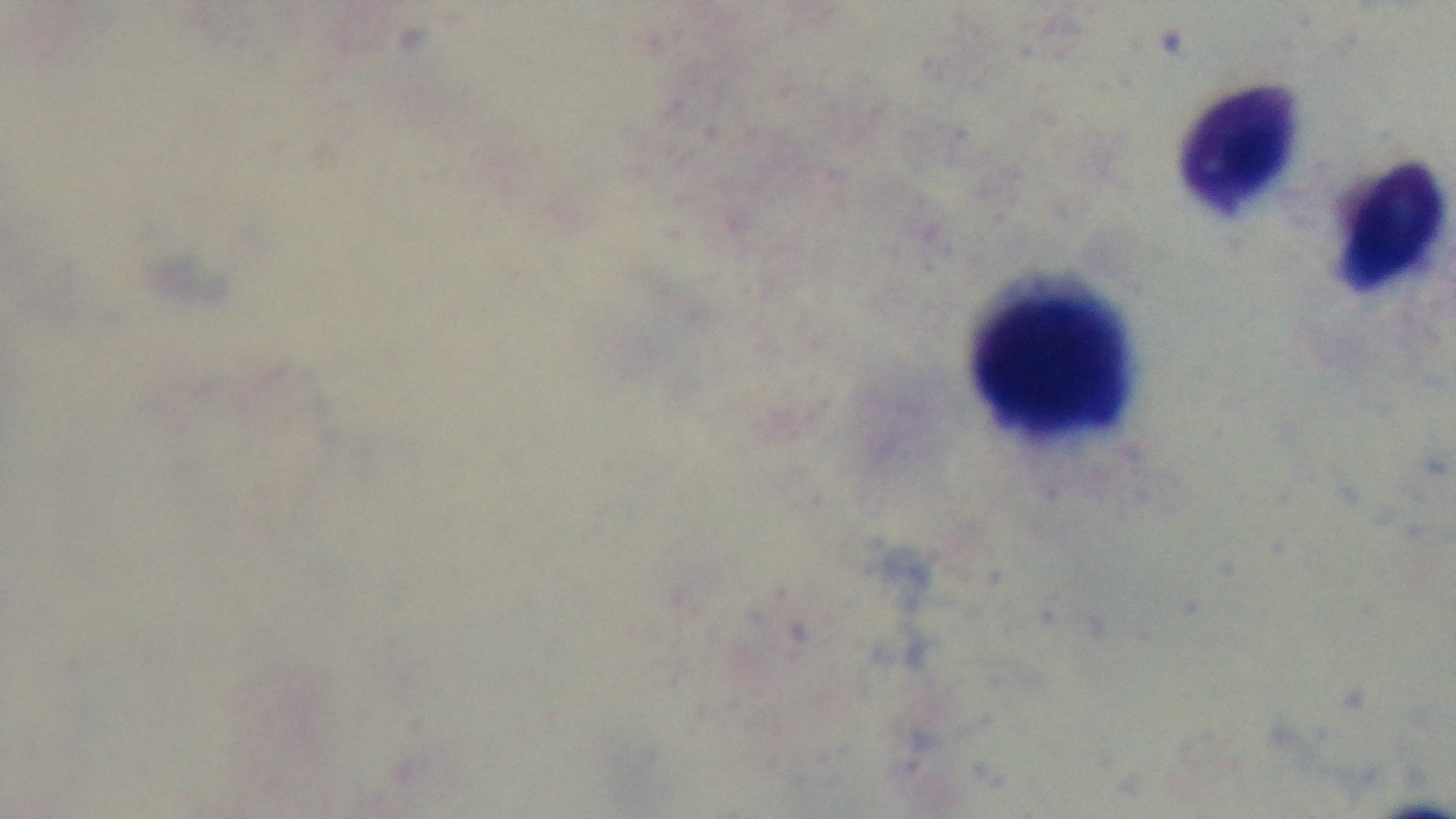
preparation = thick smear
objective = 100x oil immersion
stain = Giemsa
capture = mounted 4K digital camera
modality = light microscopy
malaria status = uninfected
field of view = single